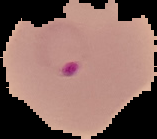

Summary:
  - Image type: cell region segmented out of the field of view; surrounding area masked to black
  - Preparation: thin blood smear
  - Malaria status: parasitized
  - Image size: 157×139 pixels